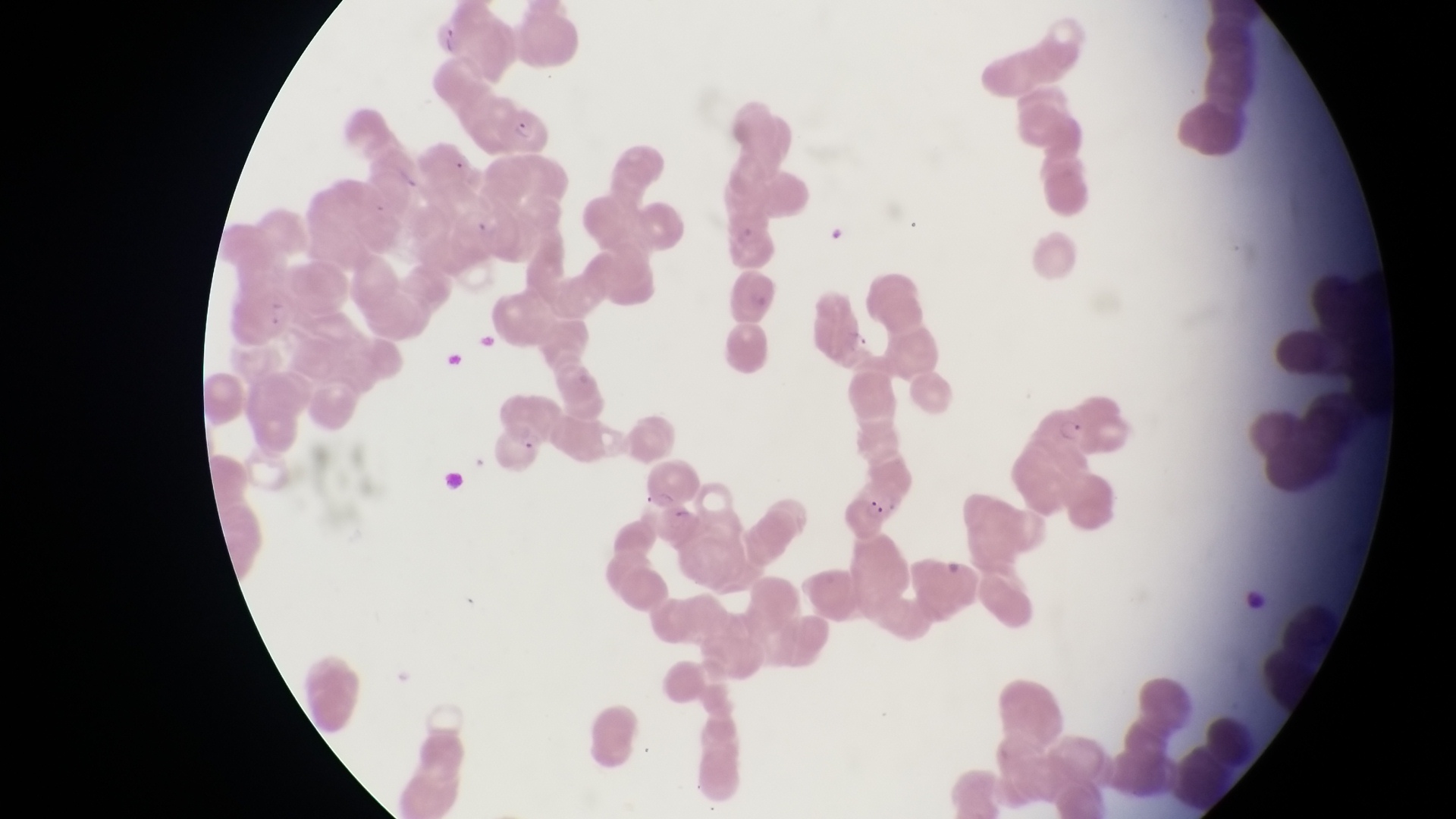

Approximate bounding boxes as {left, top, right, bottom} in pixels. Parasitised red blood cell locations: {494, 102, 554, 154}, {1036, 394, 1096, 453}, {839, 491, 895, 540}. Collected in Uganda. Captured by a smartphone held over the eyepiece of an Olympus CX-23 microscope. Magnification of 1000x. Single field of view. Thin blood film. Image is 1456×819 pixels.